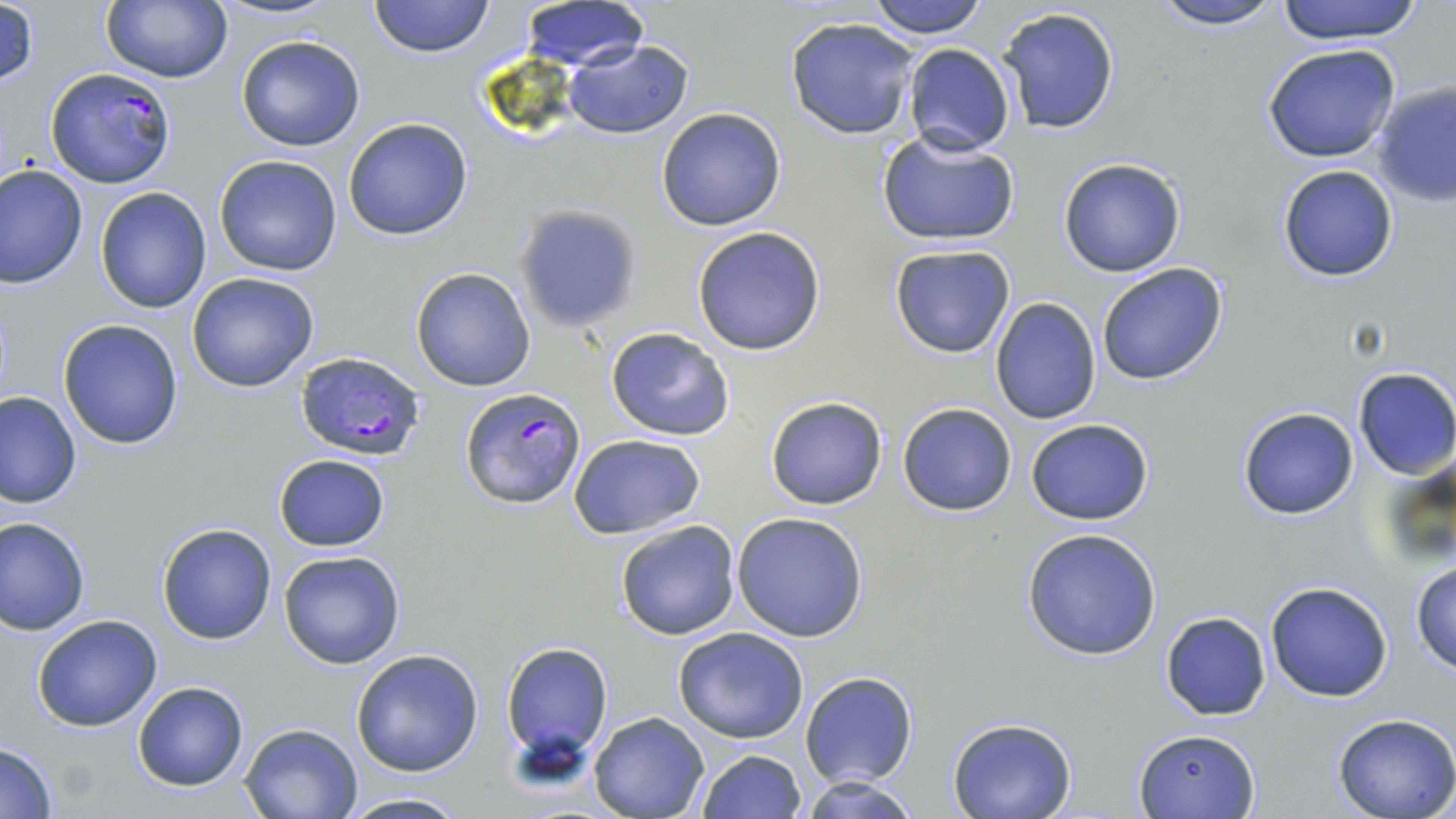

Approximate bounding boxes as [x1, y1, x2, y2] in pixels. Uninfected red blood cell locations: [369, 0, 494, 58], [865, 0, 992, 39], [1146, 0, 1285, 29], [1271, 0, 1429, 45], [100, 2, 233, 84], [518, 2, 650, 69], [996, 5, 1122, 137], [784, 16, 921, 140], [236, 34, 366, 151], [562, 39, 694, 139], [901, 43, 1015, 156], [1262, 43, 1403, 163], [1372, 80, 1455, 209], [656, 107, 787, 230], [341, 117, 473, 240], [876, 130, 1019, 246], [213, 155, 344, 277], [1057, 158, 1186, 278], [0, 164, 87, 288], [1278, 165, 1398, 282], [94, 188, 212, 313], [512, 203, 643, 332], [692, 226, 827, 356], [888, 243, 1016, 359], [1095, 263, 1231, 386], [410, 267, 536, 392], [185, 273, 321, 393], [989, 297, 1101, 424], [57, 318, 185, 450], [605, 327, 735, 441], [1352, 367, 1456, 481], [0, 389, 80, 508], [764, 394, 889, 512], [896, 403, 1017, 516], [1237, 407, 1359, 520], [1025, 419, 1154, 525], [569, 433, 706, 538], [272, 454, 391, 552], [732, 512, 871, 642], [1, 517, 89, 635], [614, 520, 741, 641], [156, 523, 276, 645], [1020, 528, 1162, 660], [278, 549, 406, 669], [1409, 561, 1456, 674], [1265, 580, 1393, 702], [1160, 611, 1271, 720], [31, 614, 164, 731], [672, 627, 811, 745], [501, 642, 613, 768], [351, 647, 484, 776], [800, 672, 919, 789], [131, 682, 250, 791], [588, 712, 709, 819], [1332, 714, 1456, 819], [947, 717, 1077, 819], [238, 721, 365, 818], [1133, 726, 1260, 816], [0, 742, 59, 818], [694, 749, 808, 819], [802, 775, 921, 819], [335, 793, 472, 819]. Plasmodium falciparum-infected red blood cell locations: [45, 68, 177, 189], [294, 350, 427, 463], [458, 386, 587, 509]. Slide-level diagnosis: Plasmodium falciparum. Optical microscopy. Thin blood smear. Single field of view. Image is 1456×819 pixels. 1000x magnification. May-Grünwald-Giemsa-stained preparation.